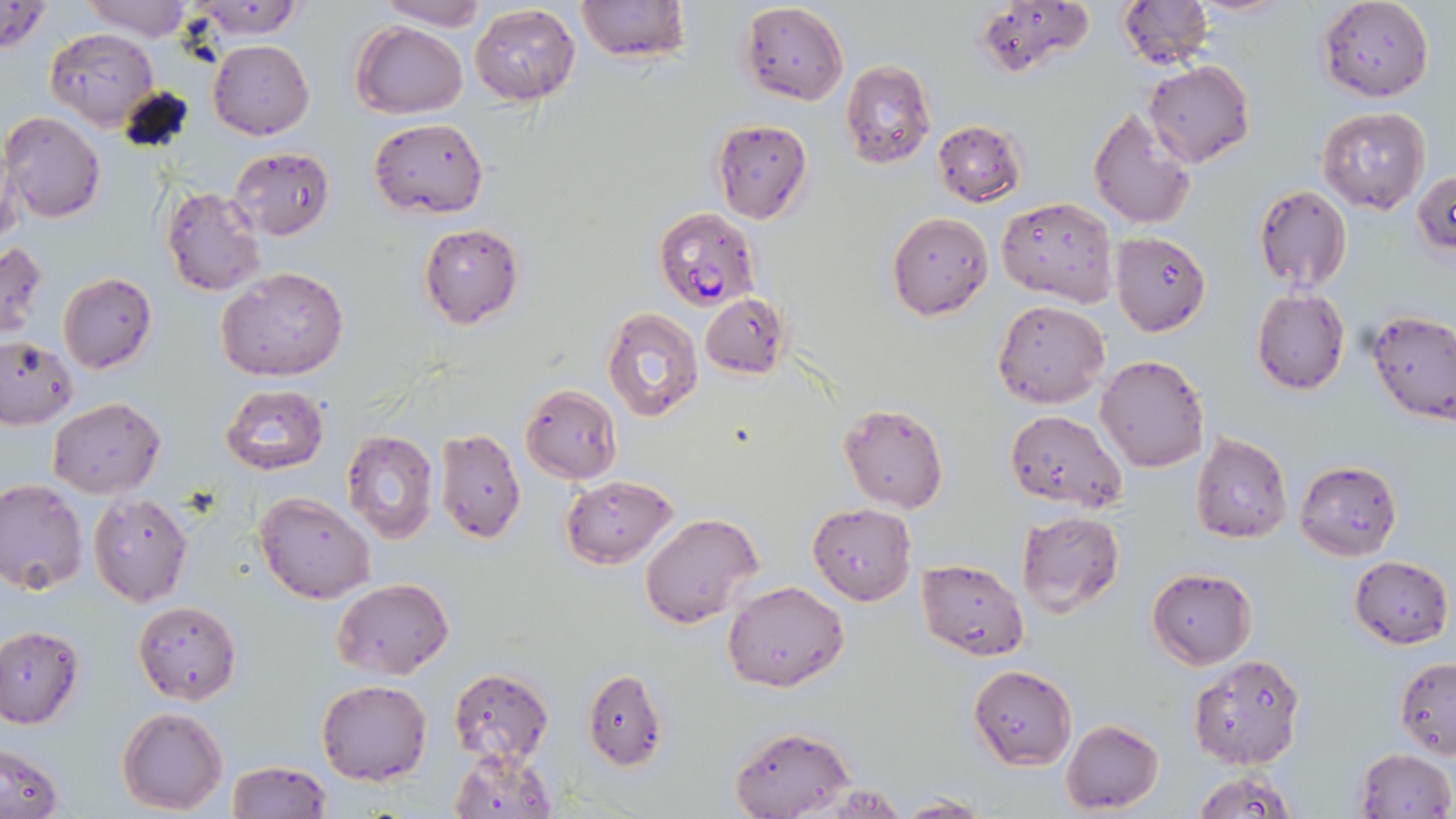
Summary:
  - Coordinate format: approximate bounding boxes as (x1, y1, x2, y2) in pixels
  - Uninfected red blood cell locations: (0, 0, 52, 56), (81, 0, 195, 40), (183, 0, 307, 40), (374, 0, 490, 30), (574, 0, 690, 63), (1117, 0, 1213, 67), (1189, 0, 1296, 17), (1317, 1, 1435, 102), (738, 2, 850, 104), (973, 2, 1095, 79), (469, 3, 581, 104), (351, 21, 468, 119), (45, 28, 160, 130), (208, 38, 314, 140), (840, 60, 936, 167), (1143, 61, 1255, 168), (1087, 107, 1197, 231), (1318, 108, 1431, 215), (2, 111, 106, 223), (368, 116, 489, 219), (710, 119, 813, 224), (932, 120, 1029, 207), (0, 139, 23, 253), (228, 147, 336, 240), (1413, 170, 1456, 258), (1252, 184, 1353, 294), (160, 185, 266, 297), (997, 196, 1118, 307), (887, 211, 993, 321), (418, 222, 525, 330), (1110, 231, 1210, 336), (0, 240, 49, 339), (216, 266, 350, 383), (58, 273, 156, 374), (1252, 289, 1350, 396), (703, 296, 792, 381), (992, 298, 1109, 409), (602, 308, 704, 423), (1365, 311, 1456, 424), (0, 336, 77, 430), (1096, 355, 1210, 474), (219, 383, 331, 475), (520, 383, 623, 484), (47, 397, 166, 499), (838, 402, 950, 514), (1004, 409, 1128, 513), (435, 426, 526, 543), (342, 430, 439, 544), (1190, 431, 1293, 544), (1296, 460, 1402, 562), (560, 474, 677, 569), (0, 478, 87, 596), (88, 493, 194, 607), (253, 493, 376, 603), (808, 502, 917, 604), (1016, 510, 1124, 618), (640, 511, 763, 628), (1348, 555, 1453, 649), (917, 557, 1029, 660), (1147, 568, 1256, 669), (332, 578, 454, 678), (723, 579, 848, 691), (133, 600, 240, 704), (0, 625, 83, 728), (1188, 653, 1304, 770), (1393, 657, 1456, 757), (967, 664, 1077, 769), (447, 668, 556, 762), (582, 669, 668, 771), (316, 679, 433, 785), (118, 707, 229, 814), (1061, 720, 1165, 814), (728, 723, 852, 818), (1, 744, 65, 818), (448, 747, 558, 818), (1353, 748, 1454, 819), (226, 760, 330, 818), (1188, 768, 1299, 819), (820, 782, 911, 818), (896, 795, 988, 817)
  - Plasmodium falciparum-infected red blood cell locations: (653, 207, 762, 310)
  - Slide-level diagnosis: Plasmodium falciparum
  - Modality: light microscopy
  - Image size: 1456×819 pixels
  - Stain: May-Grünwald-Giemsa
  - Preparation: thin blood film
  - Field of view: single
  - Magnification: 1000x